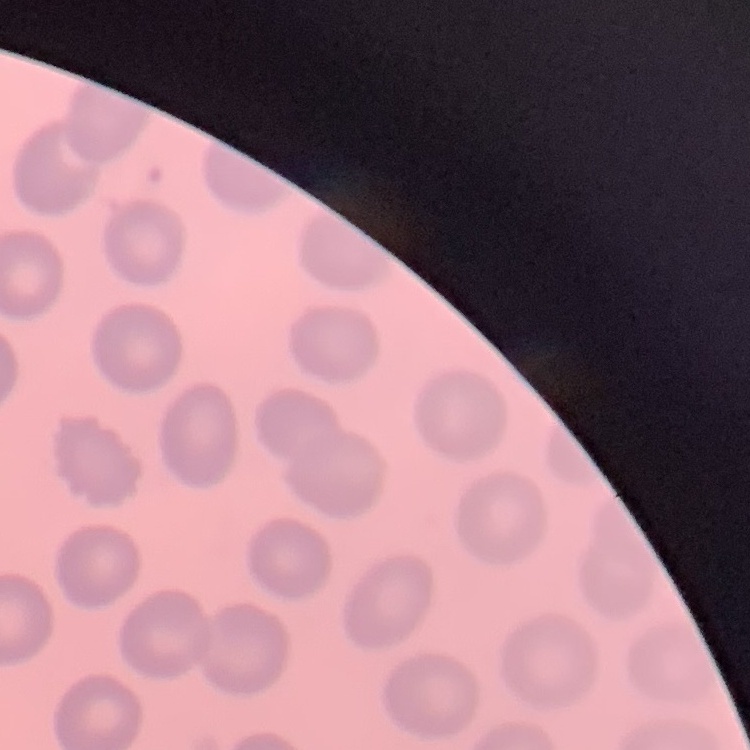
erythrocyte morphology = no rouleaux formation
image type = square crop of a larger photomicrograph
preparation = thin blood smear
stain = Field's or Giemsa